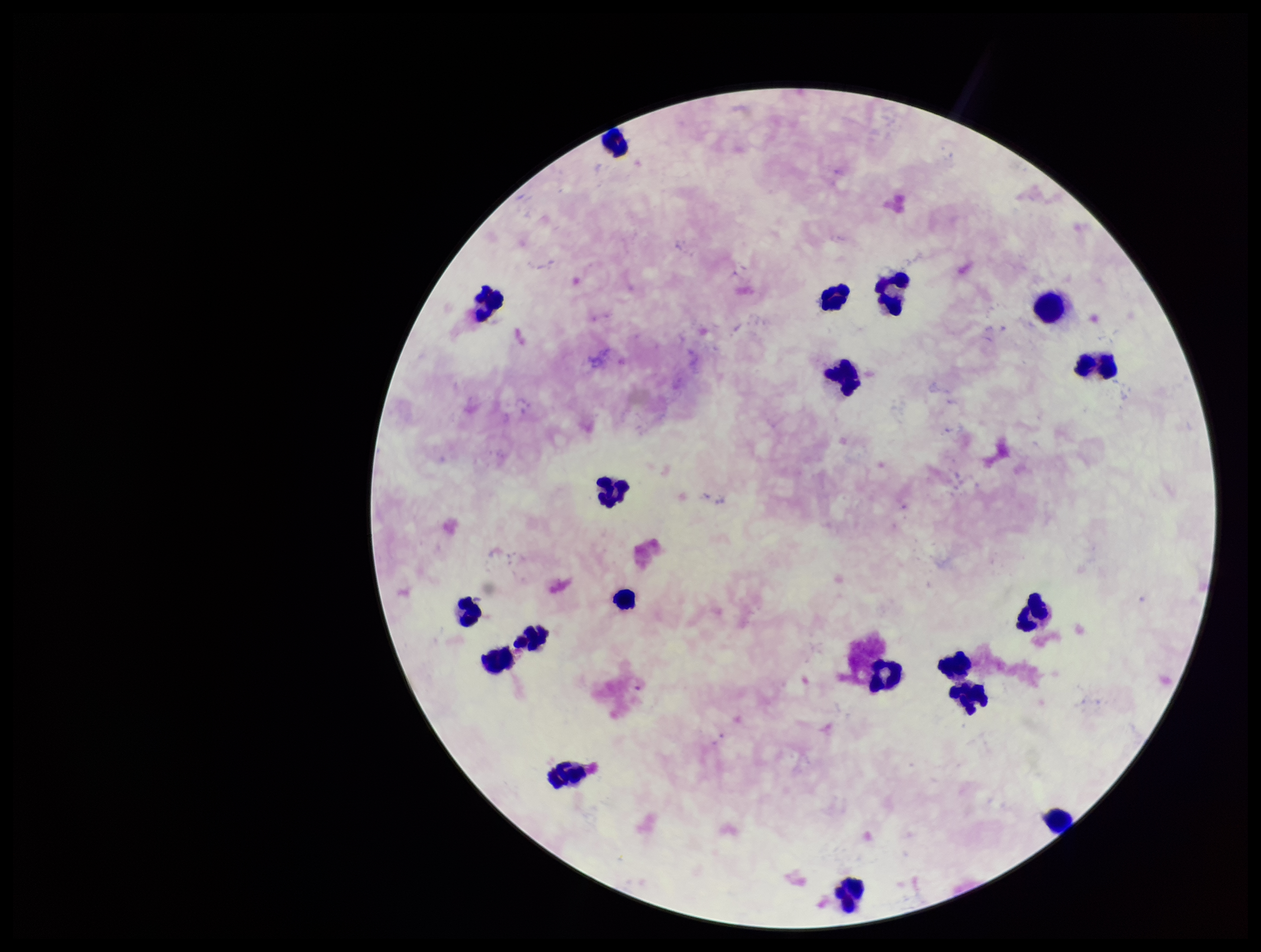 Preparation: thick. Plasmodium parasites: none seen. Single field of view. Leukocyte count: 19. Image is 1261×952 pixels. Parasite count: 0. Smartphone photograph taken through the eyepiece of a microscope. Patient malaria status: negative. Giemsa stain.